Assess the morphology of the red blood cells.
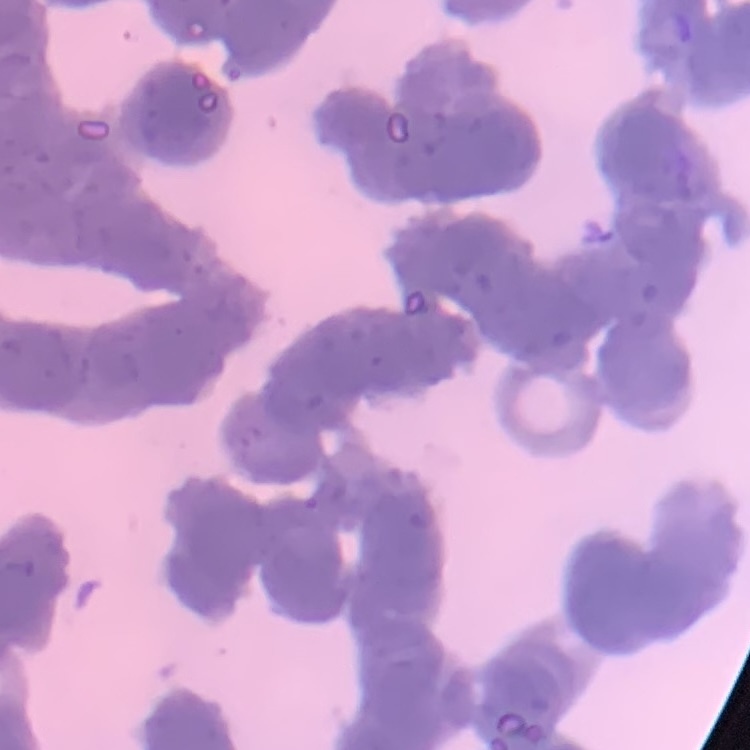
They show rouleaux formation.

Stained with either Field's or Giemsa. Thin blood smear. One tile cut from a larger photomicrograph.